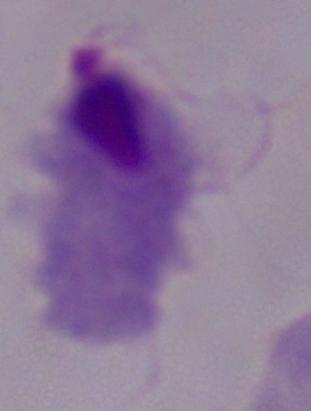

Photomicrograph. A trichomonad is seen. Captured at 1000x magnification.